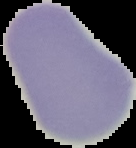

Summary:
  - Malaria status: uninfected
  - Image type: segmented cell region with the area outside set to black
  - Preparation: thin blood smear
  - Image size: 136×148 pixels